Classify this cell by malaria status.
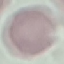
It is uninfected.

Photographed with a smartphone camera at the microscope eyepiece. Automatically extracted cell patch, resized to 64 × 64 pixels. Thin blood smear. Giemsa stain.